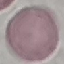

Malaria status: uninfected. Thin blood smear. Automatically extracted cell patch, resized to 64 × 64 pixels. Giemsa stain. Photographed with a smartphone camera at the microscope eyepiece.